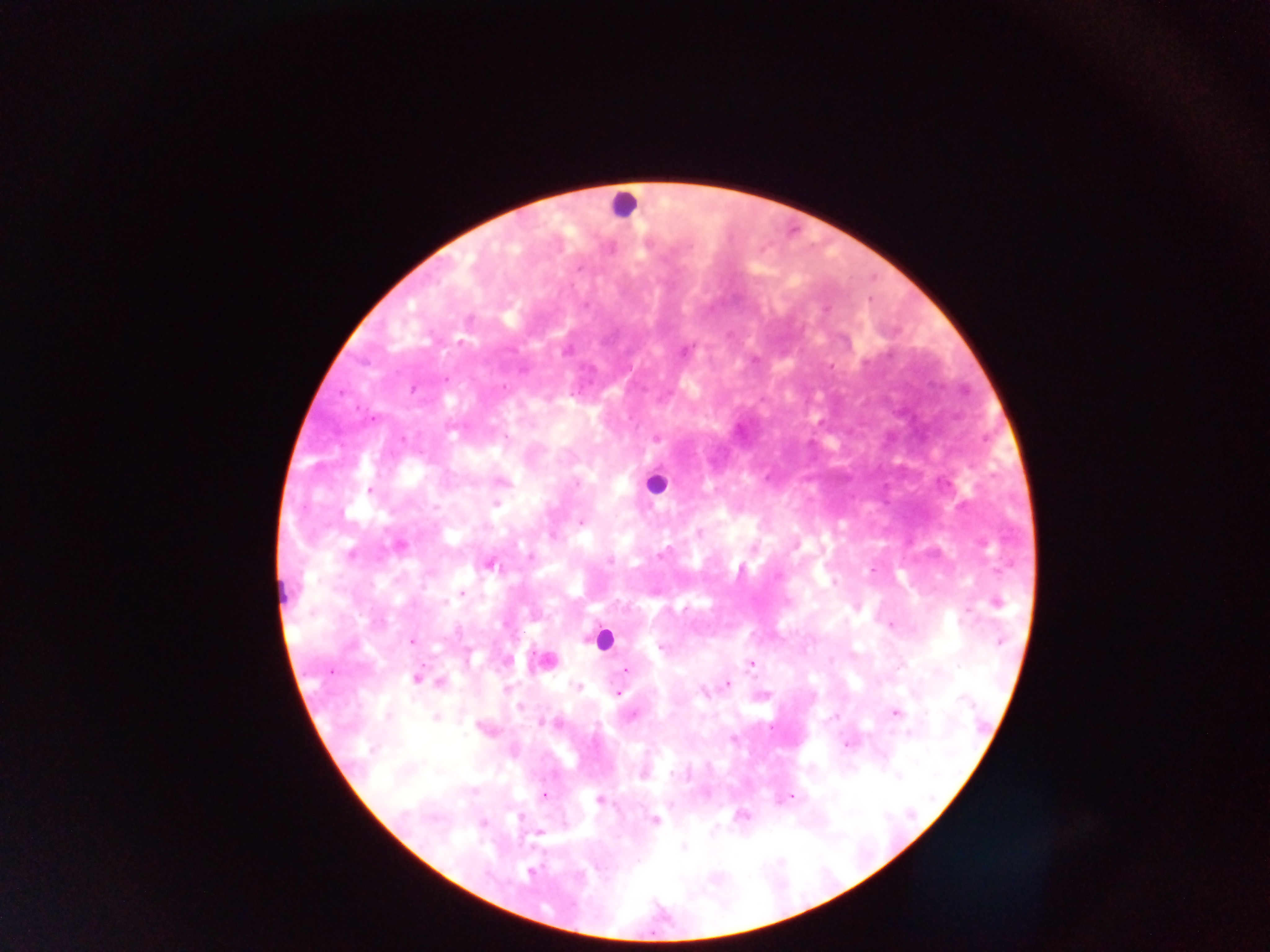

Approximate centers as [x, y] in pixels.
Summary:
  - Leukocyte locations: [624, 204], [654, 483], [602, 639]
  - Malaria parasite locations: [579, 269], [460, 342], [412, 389], [371, 419], [507, 438], [657, 438], [502, 482], [578, 484], [370, 491], [496, 504], [581, 523], [699, 532], [551, 536], [399, 546], [351, 555], [661, 555], [530, 556], [609, 561], [490, 564], [872, 570], [833, 583], [462, 593], [997, 603], [968, 613], [891, 625], [999, 641], [411, 642], [660, 647], [751, 664], [626, 670], [332, 672], [416, 679], [441, 682], [727, 684], [576, 686], [703, 692], [618, 693], [520, 707], [896, 713], [633, 715], [387, 716], [435, 717], [542, 723], [909, 733], [732, 739], [846, 745], [643, 776], [899, 776], [544, 794], [791, 796], [599, 800], [740, 815], [519, 818], [655, 820], [483, 823], [539, 833], [684, 847], [531, 873]
  - Capture: mobile-phone photograph through a microscope
  - Country: Ghana
  - Field of view: single
  - Image size: 1270×952 pixels
  - Preparation: thick blood smear